Assess this cell for malaria.
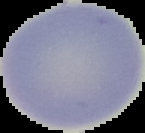
Uninfected.

Summary:
  - Image size: 145×133 pixels
  - Preparation: thin blood film
  - Image type: cell region segmented out of the field of view; surrounding area masked to black